Identify the parasite.
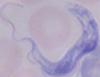
A trypanosome.

Captured at 1000x magnification. Photomicrograph.